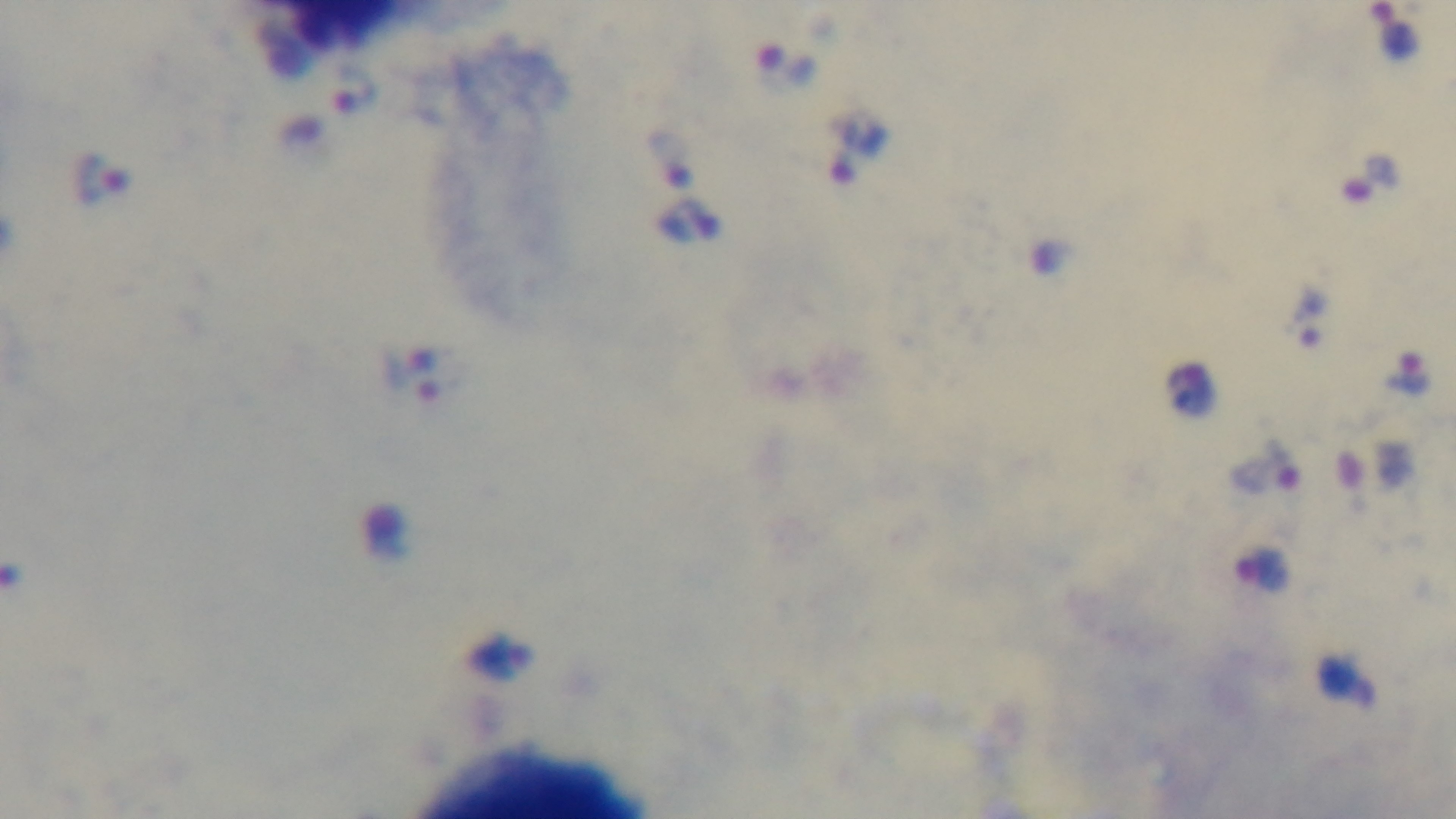
Summary:
  - Objective: 100x oil immersion
  - Capture: mounted 4K digital camera
  - Preparation: thick
  - Modality: light microscopy
  - Malaria status: infected
  - Stain: Giemsa
  - Field of view: single